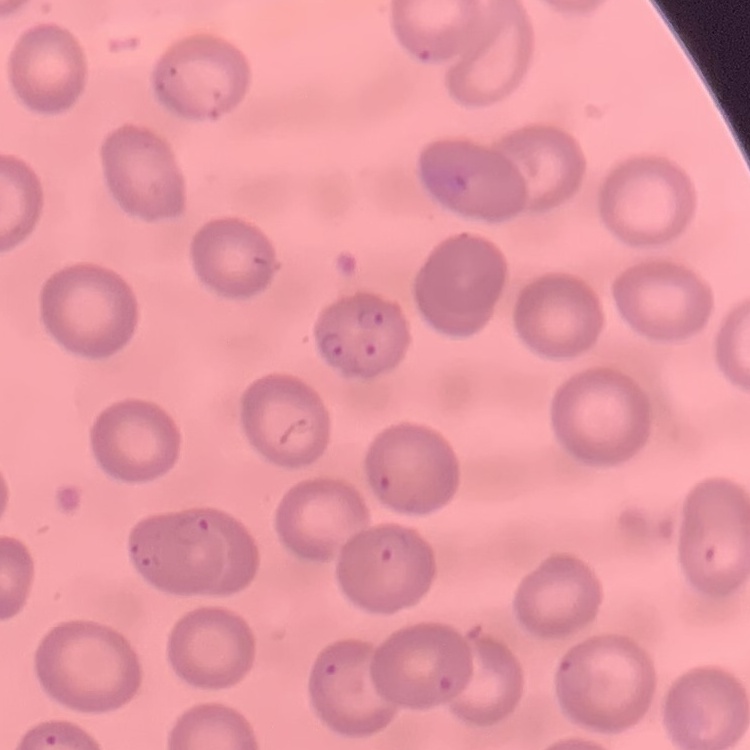

Summary:
  - Red blood cell morphology: no rouleaux formation
  - Preparation: thin blood film
  - Stain: Field's or Giemsa
  - Image type: one tile cut from a larger photomicrograph